Assess this cell for malaria.
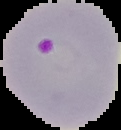
It is parasitized.

Summary:
  - Image type: segmented cell region on a black background
  - Preparation: thin blood film
  - Image size: 121×130 pixels